Classify this cell by malaria status.
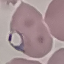

It is parasitized.

Summary:
  - Image type: automatically extracted cell patch, resized to 64 × 64 pixels
  - Stain: Giemsa
  - Capture: smartphone through the microscope eyepiece
  - Preparation: thin blood film